Name the cell type shown.
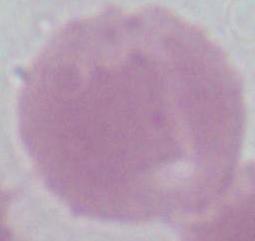

An erythrocyte.

Micrograph. 1000x magnification.